Locate every uninfected red blood cell.
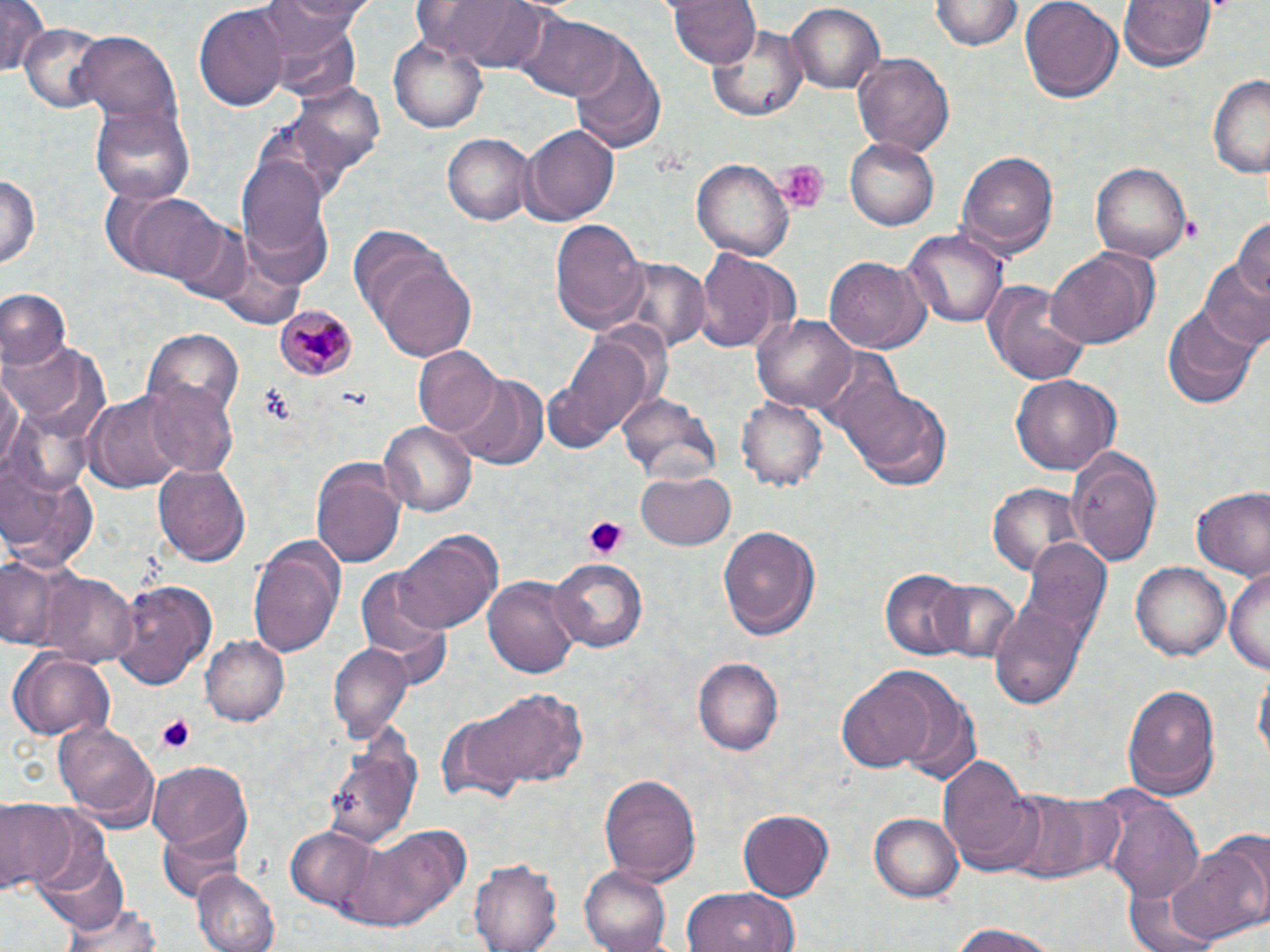
Approximate bounding boxes as (x1, y1, x2, y2) in pixels.
Uninfected red blood cells: (0, 0, 51, 76), (267, 0, 372, 42), (419, 0, 552, 72), (667, 0, 760, 72), (928, 0, 1022, 55), (1019, 0, 1123, 99), (1119, 0, 1215, 72), (192, 2, 287, 111), (785, 2, 884, 94), (515, 8, 617, 100), (707, 19, 812, 124), (20, 22, 110, 111), (75, 32, 182, 128), (388, 37, 489, 133), (570, 46, 663, 149), (852, 52, 955, 160), (1206, 70, 1270, 177), (291, 78, 388, 180), (90, 103, 196, 208), (520, 125, 620, 224), (442, 132, 536, 226), (845, 136, 942, 231), (958, 150, 1059, 258), (238, 154, 330, 255), (692, 155, 795, 260), (1092, 159, 1192, 260), (0, 169, 41, 275), (116, 192, 227, 283), (1232, 215, 1270, 301), (548, 218, 647, 333), (903, 230, 1006, 328), (1045, 247, 1155, 351), (695, 249, 789, 351), (824, 257, 930, 353), (612, 258, 709, 353), (375, 259, 479, 363), (1200, 263, 1270, 353), (983, 280, 1090, 385), (1, 289, 71, 368), (1159, 299, 1265, 410), (750, 312, 859, 413), (143, 329, 243, 425), (545, 331, 658, 450), (5, 340, 106, 438), (413, 347, 502, 439), (0, 366, 23, 480), (454, 373, 546, 467), (1011, 375, 1120, 475), (140, 377, 236, 477), (845, 380, 952, 488), (86, 390, 189, 493), (617, 390, 724, 487), (738, 393, 827, 491), (381, 419, 476, 516), (1067, 446, 1166, 567), (1, 460, 100, 574), (152, 463, 251, 565), (311, 464, 405, 569), (636, 472, 736, 551), (988, 482, 1085, 580), (1189, 486, 1269, 580), (718, 525, 818, 640), (395, 532, 502, 636), (1016, 533, 1111, 654), (248, 537, 343, 661), (1, 554, 87, 655), (549, 556, 646, 651), (1131, 562, 1230, 663), (356, 566, 456, 678), (1224, 566, 1268, 674), (881, 570, 968, 657), (41, 573, 139, 667), (484, 574, 583, 681), (112, 578, 218, 692), (929, 579, 1022, 663), (990, 603, 1089, 711), (201, 632, 289, 724), (329, 643, 411, 742), (5, 648, 114, 740), (693, 657, 783, 757), (1253, 665, 1269, 770), (886, 673, 983, 787), (837, 674, 938, 774), (1122, 682, 1221, 799), (473, 686, 586, 791), (437, 710, 525, 804), (54, 719, 159, 826), (323, 728, 422, 851), (938, 750, 1038, 872), (149, 762, 252, 854), (598, 772, 702, 886), (1003, 790, 1118, 883), (1105, 795, 1205, 902), (1, 800, 75, 892), (738, 809, 835, 900), (867, 811, 964, 901), (343, 825, 468, 934), (155, 826, 245, 904), (286, 826, 385, 915), (1167, 841, 1269, 943), (39, 847, 131, 936), (471, 858, 563, 952), (580, 866, 672, 952), (194, 868, 280, 952), (681, 887, 799, 952), (63, 898, 165, 952), (947, 921, 1060, 952).

{
  "slide_level_diagnosis": "Plasmodium malariae",
  "modality": "light microscopy",
  "image_size": "1270×952 pixels",
  "stain": "May-Grünwald-Giemsa",
  "platelet_locations": "approximate bounding boxes as (x1, y1, x2, y2) in pixels: (777, 158, 831, 213), (583, 517, 630, 560), (154, 714, 199, 755)",
  "preparation": "thin blood film",
  "plasmodium_malariae_infected_red_blood_cell_locations": "approximate bounding boxes as (x1, y1, x2, y2) in pixels: (272, 306, 357, 381)",
  "magnification": "1000x",
  "field_of_view": "single"
}